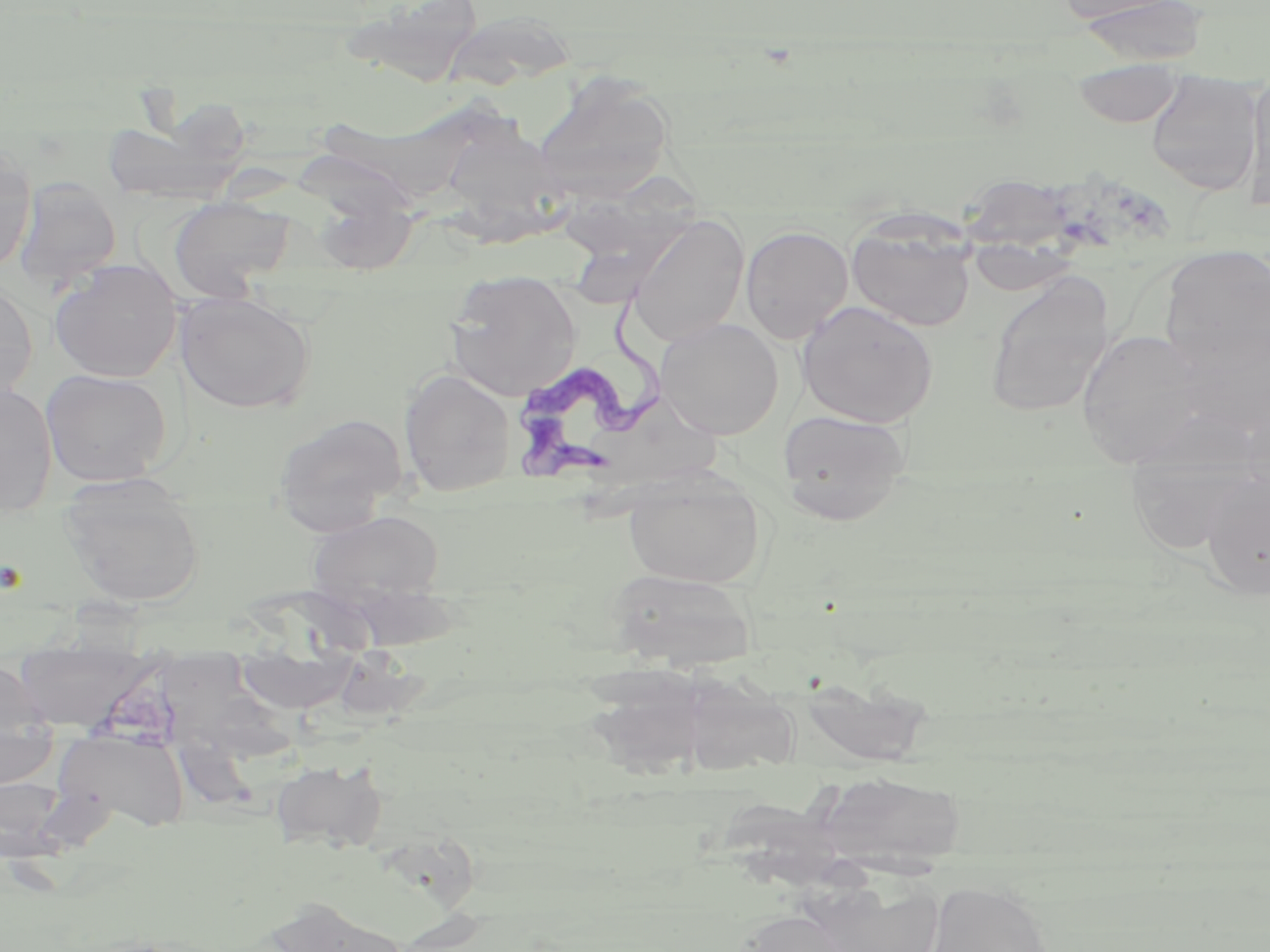
{
  "slide_level_diagnosis": "Trypanosoma brucei",
  "magnification": "1000x",
  "field_of_view": "single",
  "uninfected_red_blood_cell_locations": "approximate bounding boxes as (x1, y1, x2, y2) in pixels: (1054, 0, 1187, 25), (1072, 0, 1209, 67), (339, 1, 484, 87), (442, 10, 577, 90), (1072, 61, 1184, 129), (1145, 72, 1263, 194), (1246, 72, 1270, 207), (532, 73, 675, 197), (305, 100, 495, 201), (451, 109, 578, 244), (0, 147, 36, 274), (560, 172, 706, 307), (13, 178, 122, 289), (968, 180, 1087, 296), (313, 190, 420, 277), (168, 196, 296, 299), (626, 215, 750, 347), (846, 217, 976, 332), (740, 225, 853, 343), (1158, 245, 1269, 375), (49, 259, 182, 383), (445, 270, 581, 400), (985, 273, 1114, 417), (0, 280, 37, 402), (176, 292, 315, 413), (797, 301, 938, 427), (656, 318, 784, 439), (1173, 320, 1270, 441), (1077, 328, 1214, 464), (399, 368, 516, 496), (41, 369, 173, 486), (0, 382, 58, 512), (777, 408, 911, 525), (272, 412, 408, 534), (1124, 460, 1260, 555), (623, 471, 766, 589), (1200, 473, 1270, 600), (59, 475, 206, 607), (306, 509, 445, 606), (606, 568, 757, 670), (13, 638, 155, 731), (0, 659, 49, 734), (672, 667, 800, 779), (585, 669, 716, 780), (796, 675, 932, 767), (57, 731, 190, 832), (0, 733, 60, 789), (270, 758, 387, 852), (817, 771, 967, 873), (0, 776, 66, 861), (812, 877, 946, 952), (924, 879, 1055, 952), (743, 912, 856, 952)",
  "modality": "light microscopy",
  "trypanosoma_brucei_locations": "approximate bounding boxes as (x1, y1, x2, y2) in pixels: (504, 276, 666, 488)",
  "stain": "May-Grünwald-Giemsa",
  "image_size": "1270×952 pixels",
  "preparation": "thin blood smear"
}